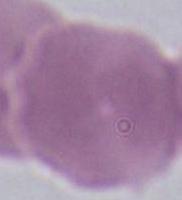

Photomicrograph. Captured at 1000x magnification. A red blood cell is seen.